Assess this cell for malaria.
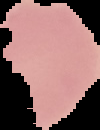
It is uninfected.

preparation = thin blood smear
image type = cell region segmented out of the field of view; surrounding area masked to black
image size = 100×130 pixels